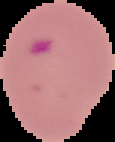

Result: Plasmodium parasites detected. Segmented cell region on a black background. From a thin blood film. Image is 115×142 pixels.